Locate every malaria parasite and every leukocyte.
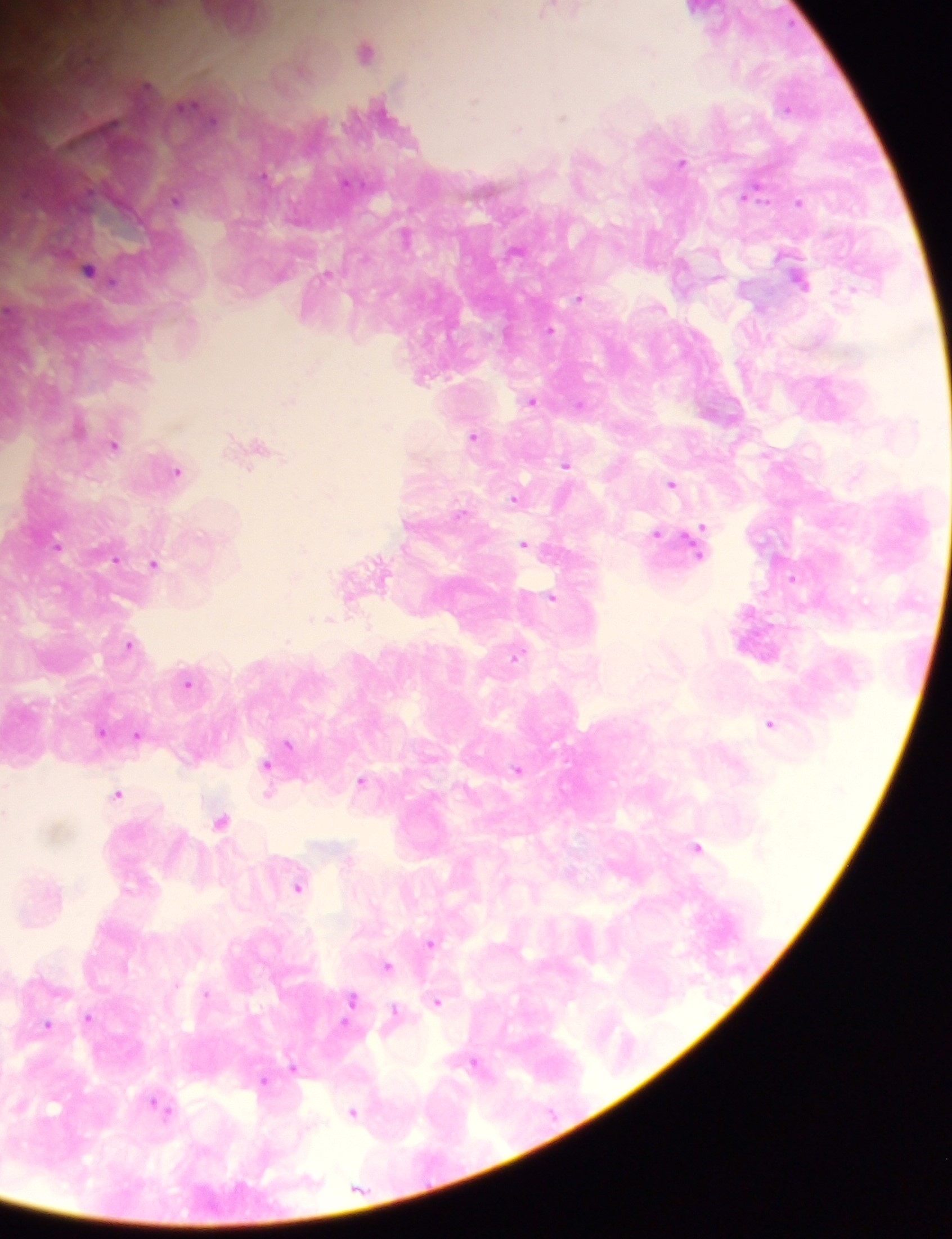
Approximate centers as {x, y} in pixels.
Malaria parasites: {789, 107}, {562, 117}, {518, 127}, {264, 173}, {176, 199}, {798, 203}, {551, 330}, {533, 399}, {580, 404}, {472, 435}, {115, 443}, {565, 467}, {672, 483}, {514, 499}, {703, 527}, {658, 533}, {525, 544}, {154, 562}, {385, 570}, {792, 577}, {553, 599}, {868, 604}, {312, 617}, {329, 617}, {287, 641}, {129, 644}, {516, 657}, {189, 684}, {771, 722}, {102, 732}, {139, 734}, {288, 743}, {267, 765}, {518, 769}, {362, 779}, {303, 780}, {270, 793}, {119, 795}, {221, 820}, {698, 846}, {298, 888}, {428, 941}, {433, 945}, {387, 965}, {177, 982}, {207, 994}, {353, 1001}, {439, 1002}, {396, 1010}, {350, 1016}, {89, 1017}, {346, 1023}, {47, 1025}, {477, 1062}, {294, 1067}, {264, 1080}, {154, 1103}, {54, 1106}, {168, 1110}, {354, 1111}.
No leukocytes observed.

preparation = thick blood film
field of view = single
country = Ghana
image size = 952×1239 pixels
capture = mobile-phone photograph through a microscope